Identify the parasite.
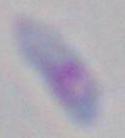
Toxoplasma gondii.

Summary:
  - Magnification: 1000x
  - Modality: photomicrograph